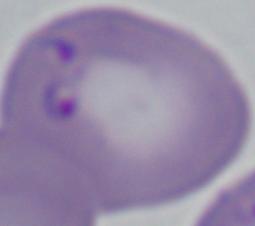 Micrograph. Captured at 1000x magnification. A Babesia parasite is seen.